Locate the red blood cells and classify each one as Plasmodium falciparum-infected, uninfected, or of indeterminate infection status.
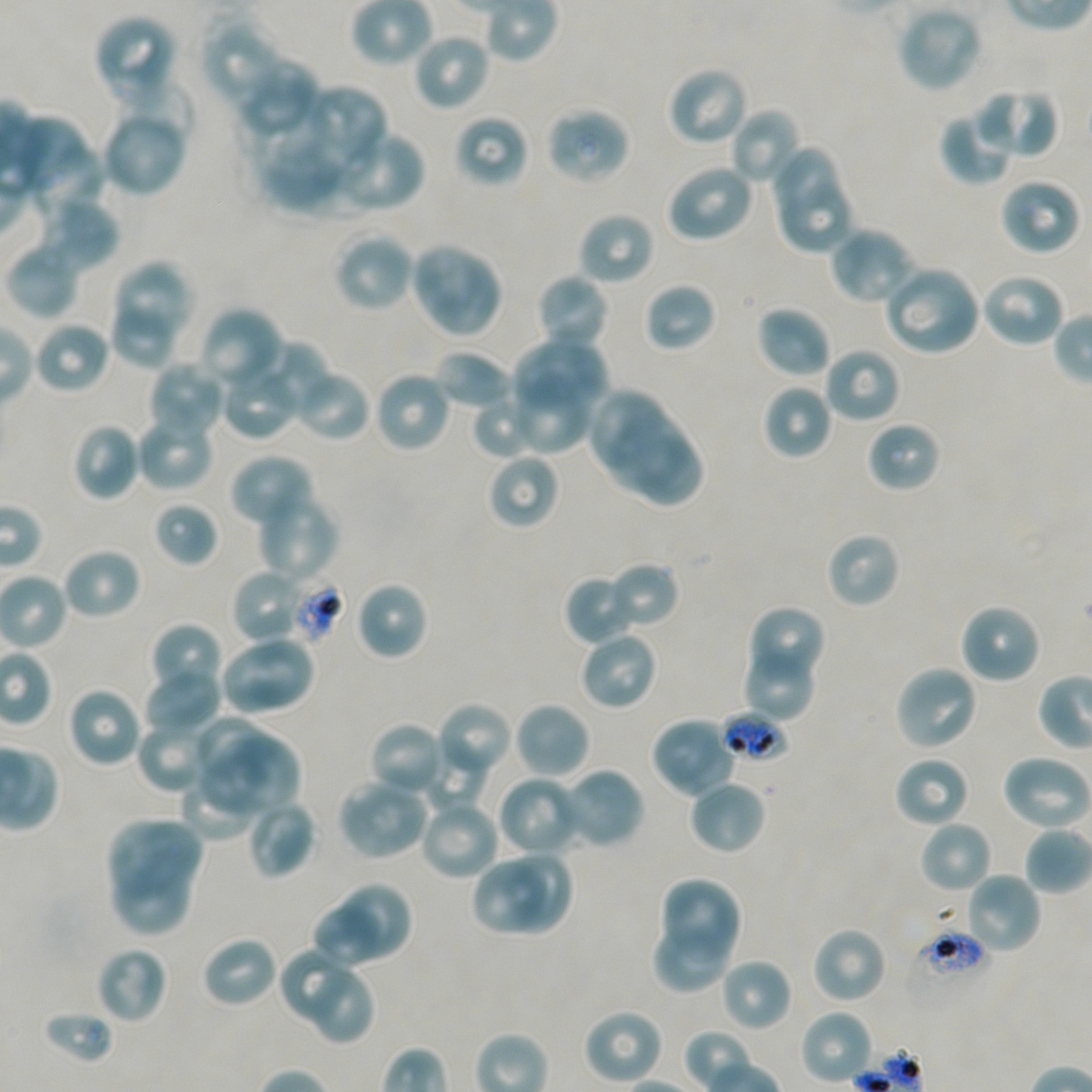

Approximate bounding boxes as [x1, y1, x2, y2] in pixels. Not every red blood cell is marked. A life-cycle stage — or a range of stages, where the recorded stages span more than one — follows each staged infected red blood cell.
Infected red blood cells: [720, 710, 788, 763] early trophozoite.
Red blood cells of indeterminate infection status: [284, 573, 345, 647], [908, 930, 989, 1002].
Uninfected red blood cells: [896, 6, 983, 94], [94, 14, 175, 84], [204, 28, 279, 99], [417, 37, 488, 109], [108, 53, 179, 104], [240, 62, 315, 133], [674, 71, 743, 141], [117, 77, 197, 145], [973, 87, 1058, 159], [310, 88, 386, 164], [729, 107, 803, 187], [939, 109, 1016, 186], [101, 112, 186, 198], [550, 113, 625, 183], [16, 120, 88, 194], [462, 120, 523, 181], [304, 122, 374, 188], [341, 134, 422, 208], [33, 145, 106, 221], [261, 147, 338, 206], [774, 150, 836, 217], [666, 163, 755, 244], [781, 183, 853, 255], [1005, 184, 1077, 251], [43, 197, 119, 274], [577, 211, 655, 287], [833, 230, 911, 299], [333, 231, 415, 312], [5, 241, 80, 319], [409, 242, 503, 338], [113, 261, 193, 337], [888, 270, 977, 352], [979, 272, 1067, 349], [541, 276, 606, 348], [647, 287, 714, 346], [755, 305, 833, 380], [198, 306, 285, 397], [115, 307, 170, 367], [33, 320, 111, 395], [515, 338, 608, 410], [255, 341, 333, 416], [433, 350, 511, 410], [826, 353, 896, 420], [148, 361, 225, 441], [290, 367, 371, 442], [374, 370, 453, 453], [225, 371, 295, 439], [509, 372, 591, 454], [761, 383, 834, 460], [470, 391, 539, 459], [590, 392, 661, 472], [605, 410, 682, 490], [135, 413, 215, 492], [865, 420, 942, 494], [71, 422, 141, 501], [637, 433, 702, 506], [229, 452, 316, 532], [492, 458, 554, 526], [261, 496, 340, 583], [153, 501, 218, 566], [824, 530, 901, 609], [60, 547, 141, 621], [611, 560, 680, 632], [230, 568, 312, 648], [568, 579, 630, 642], [354, 580, 429, 661], [958, 602, 1042, 685], [746, 605, 824, 687], [156, 625, 219, 689], [578, 630, 658, 712], [217, 635, 316, 716], [747, 653, 812, 719], [893, 664, 979, 752], [144, 667, 222, 738], [66, 687, 143, 769], [512, 701, 591, 780], [440, 706, 509, 773], [196, 713, 265, 781], [136, 716, 217, 792], [655, 721, 734, 793], [373, 726, 439, 790], [224, 731, 300, 814], [424, 739, 486, 812], [1000, 753, 1091, 831], [202, 754, 273, 812], [894, 755, 970, 829], [564, 770, 641, 844], [178, 773, 257, 842], [502, 780, 575, 854], [687, 780, 766, 856], [340, 785, 424, 856], [245, 797, 317, 880], [425, 806, 495, 877], [107, 817, 208, 894], [918, 819, 994, 895], [1025, 825, 1092, 894], [506, 850, 576, 936], [473, 860, 545, 932], [111, 861, 192, 935], [964, 871, 1042, 955], [663, 877, 745, 958], [344, 881, 415, 964], [307, 901, 385, 971], [653, 920, 732, 993], [811, 926, 888, 1004], [201, 935, 278, 1009], [278, 945, 351, 1025], [95, 946, 168, 1025], [720, 958, 793, 1033], [311, 970, 377, 1047], [583, 1008, 665, 1085], [43, 1009, 114, 1065], [799, 1009, 873, 1085].

Image is 1092×1092 pixels. Thin blood film. Blood group of the donor: A+/O+. 100x objective under oil immersion, numerical aperture 1.45. Static in-vitro culture of Plasmodium falciparum strain NF54. Giemsa stain. One field from this slide.